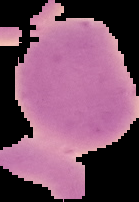
{
  "preparation": "thin blood film",
  "malaria_status": "uninfected",
  "image_size": "139×202 pixels",
  "image_type": "segmented cell region with the area outside set to black"
}